Locate every blood parasite and identify its species.
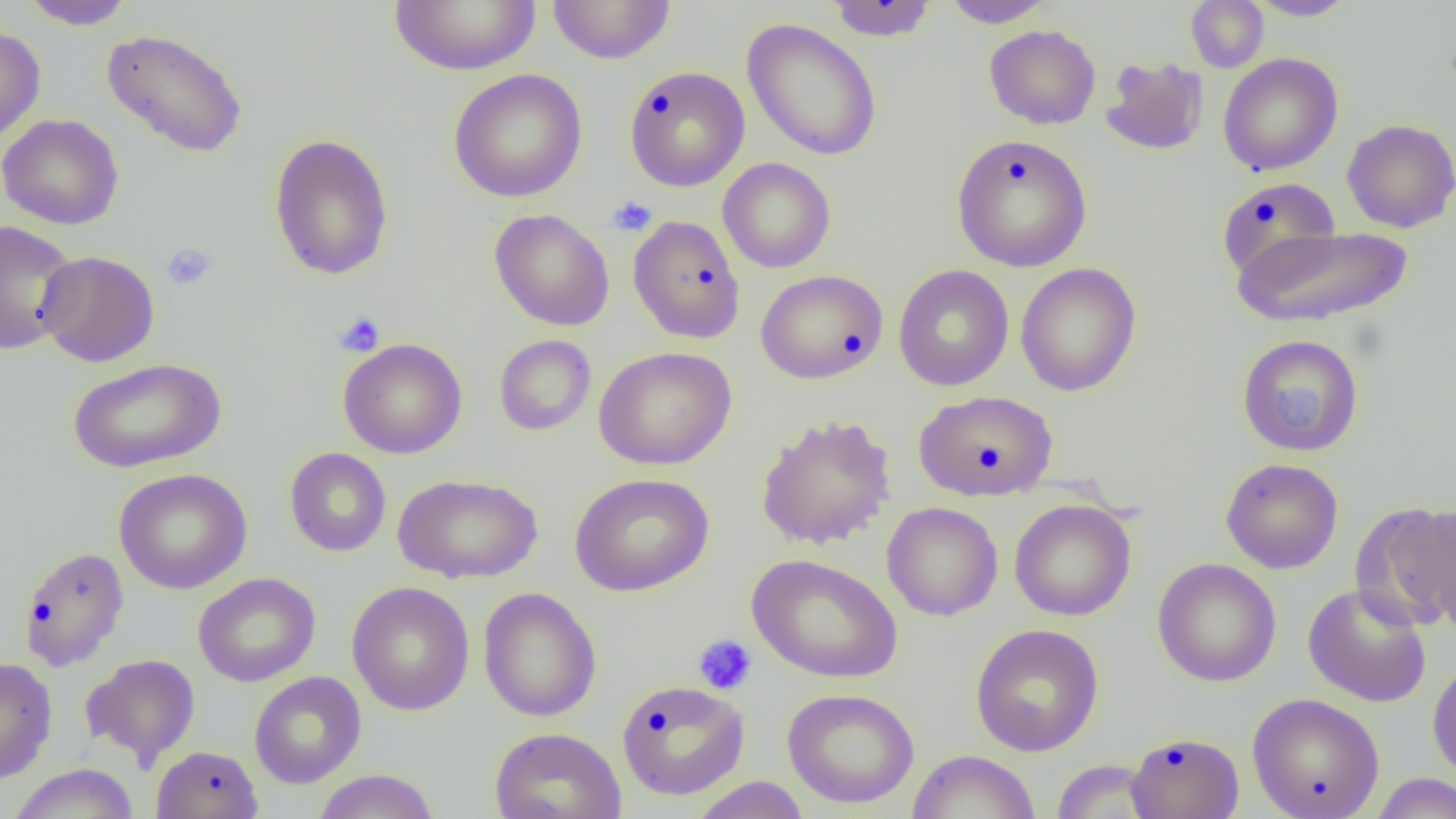

No blood parasites observed.

Summary:
  - Coordinate format: approximate bounding boxes as [x1, y1, x2, y2] in pixels
  - Platelet locations: [608, 196, 656, 236], [161, 242, 218, 290], [335, 310, 385, 357], [1267, 381, 1331, 438], [693, 634, 757, 695]
  - Uninfected red blood cell locations: [18, 0, 137, 30], [389, 0, 541, 76], [547, 0, 676, 65], [941, 0, 1055, 28], [1245, 0, 1358, 20], [826, 1, 939, 41], [1186, 1, 1269, 72], [741, 18, 882, 162], [0, 24, 46, 145], [984, 24, 1101, 129], [101, 28, 249, 158], [1218, 53, 1343, 176], [1100, 55, 1208, 156], [624, 65, 750, 191], [448, 69, 587, 203], [0, 114, 124, 230], [1341, 119, 1456, 233], [268, 133, 394, 281], [951, 133, 1092, 272], [718, 157, 836, 273], [1217, 177, 1341, 281], [489, 209, 615, 331], [628, 215, 745, 344], [0, 219, 80, 355], [1231, 225, 1414, 329], [36, 250, 160, 367], [1015, 262, 1142, 397], [893, 264, 1014, 392], [755, 269, 888, 385], [1236, 333, 1364, 457], [493, 334, 596, 436], [338, 338, 468, 459], [593, 346, 737, 470], [67, 357, 227, 474], [913, 389, 1058, 501], [755, 414, 896, 551], [285, 447, 391, 557], [1220, 458, 1344, 574], [114, 468, 252, 594], [568, 472, 714, 597], [392, 473, 543, 584], [1009, 499, 1136, 621], [882, 502, 1003, 621], [1351, 502, 1456, 630], [1409, 505, 1456, 630], [17, 546, 129, 672], [747, 554, 904, 683], [1152, 558, 1282, 687], [193, 572, 321, 687], [346, 581, 475, 715], [1303, 583, 1431, 707], [478, 587, 602, 722], [970, 623, 1104, 757], [81, 653, 200, 767], [0, 657, 57, 784], [1427, 657, 1456, 784], [249, 671, 366, 788], [616, 679, 750, 800], [782, 688, 920, 809], [1247, 692, 1385, 819], [489, 727, 627, 819], [1126, 731, 1244, 819], [151, 745, 264, 819], [908, 750, 1041, 819], [1050, 759, 1159, 818], [7, 763, 140, 819], [312, 769, 440, 819], [1369, 773, 1456, 818], [691, 776, 811, 819]
  - Slide-level diagnosis: negative for blood parasites
  - Field of view: single
  - Modality: light microscopy
  - Magnification: 1000x
  - Image size: 1456×819 pixels
  - Preparation: thin blood smear